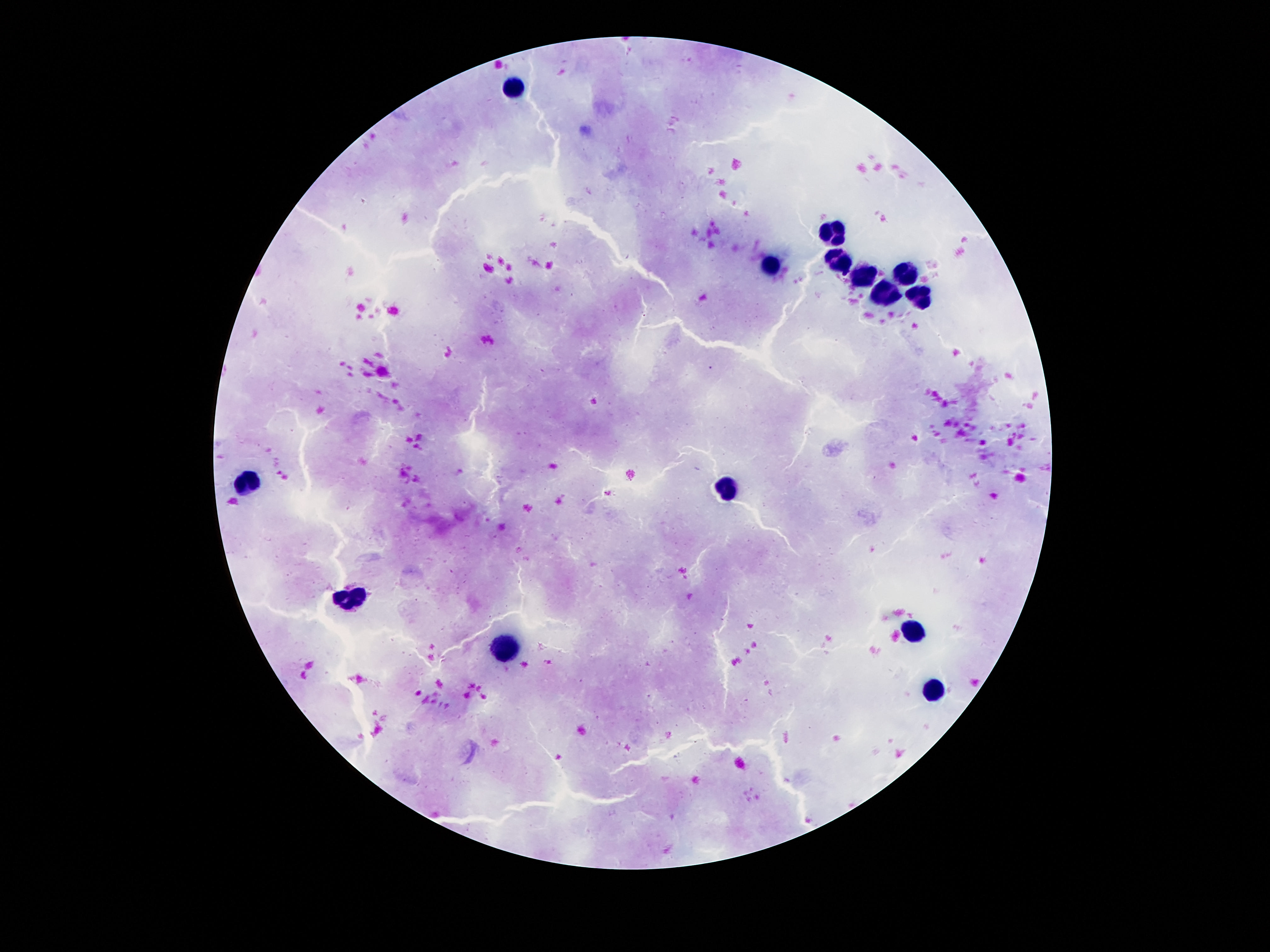 Approximate centers as (x, y) in pixels. Leukocyte locations: (511, 87), (833, 232), (839, 259), (770, 265), (864, 274), (906, 274), (885, 297), (916, 302), (247, 482), (728, 493), (354, 601), (914, 629), (505, 652), (933, 689). Photographed through the microscope eyepiece with a smartphone camera. Image is 1270×952 pixels. Thick blood smear. 100x magnification. One field from this slide. Patient malaria status: uninfected. Giemsa stain.